Identify the blood parasite species.
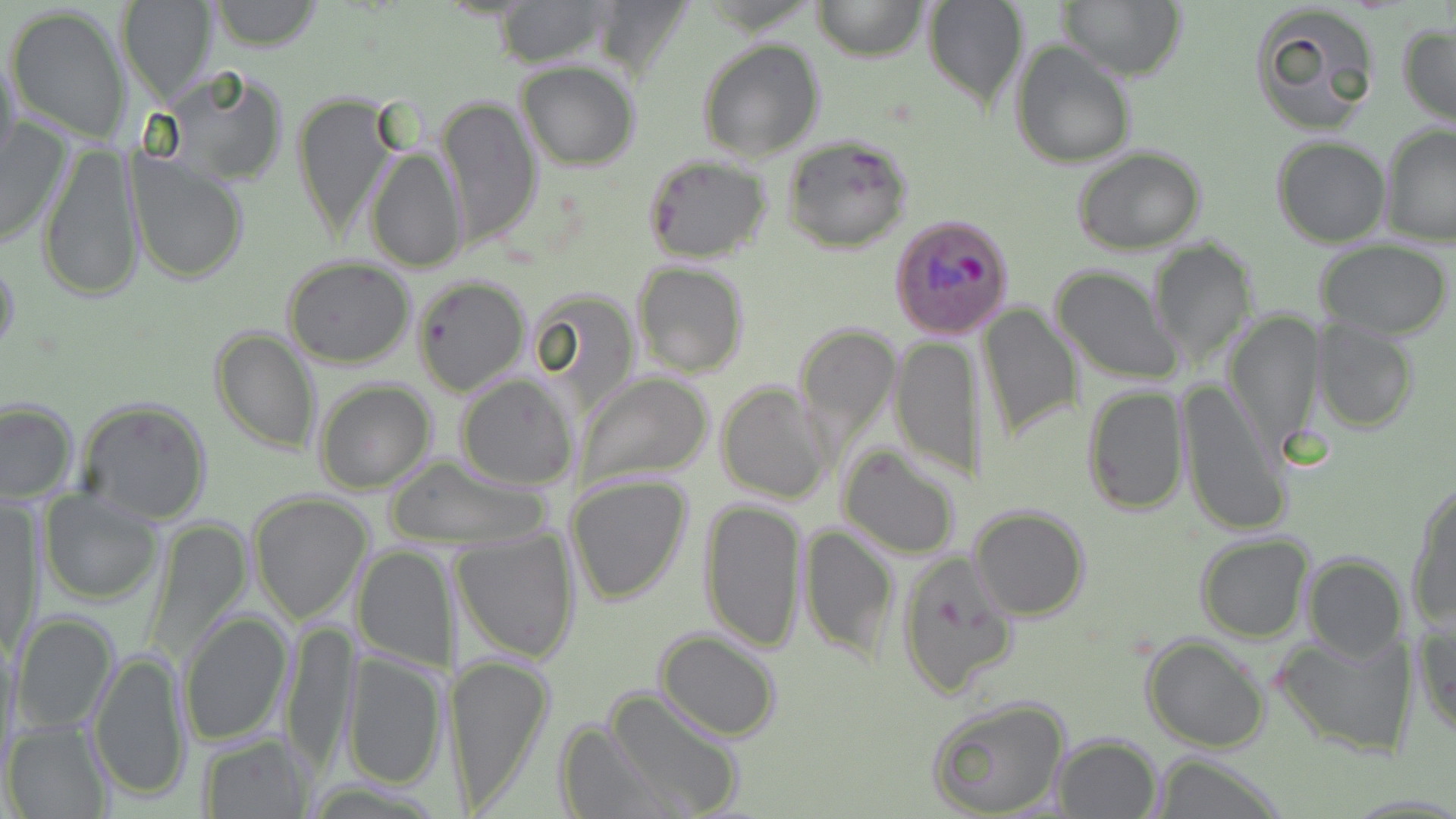

Plasmodium ovale.

modality = optical microscopy
image size = 1456×819 pixels
Plasmodium ovale-infected red blood cell locations = approximate bounding boxes as (x1, y1, x2, y2) in pixels: (891, 214, 1014, 339)
magnification = 1000x
field of view = single
preparation = thin blood film
stain = May-Grünwald-Giemsa
uninfected red blood cell locations = approximate bounding boxes as (x1, y1, x2, y2) in pixels: (207, 0, 328, 51), (493, 0, 613, 66), (588, 0, 696, 84), (812, 0, 927, 62), (920, 0, 1030, 111), (1055, 0, 1187, 83), (117, 1, 217, 105), (1248, 1, 1382, 135), (7, 5, 131, 143), (1398, 23, 1456, 127), (696, 38, 824, 163), (1011, 39, 1138, 168), (0, 44, 23, 184), (517, 62, 639, 169), (149, 65, 289, 189), (292, 93, 397, 241), (436, 95, 541, 246), (0, 117, 72, 250), (1380, 124, 1456, 246), (780, 133, 913, 254), (1270, 135, 1391, 247), (38, 139, 144, 303), (365, 147, 468, 274), (1072, 147, 1206, 256), (127, 151, 250, 283), (644, 154, 772, 264), (1150, 237, 1259, 367), (1314, 242, 1455, 339), (0, 246, 21, 371), (282, 258, 415, 369), (632, 261, 749, 378), (1052, 265, 1183, 384), (412, 273, 532, 396), (531, 290, 642, 411), (976, 302, 1081, 445), (1225, 310, 1323, 451), (1312, 318, 1419, 432), (794, 322, 902, 448), (209, 325, 320, 455), (891, 334, 983, 481), (574, 371, 714, 490), (455, 373, 580, 490), (1175, 375, 1289, 538), (313, 380, 436, 495), (715, 380, 834, 503), (1082, 385, 1189, 516), (76, 396, 214, 525), (0, 400, 79, 503), (838, 444, 962, 559), (385, 456, 552, 551), (566, 474, 693, 607), (1408, 484, 1456, 630), (40, 489, 163, 605), (247, 491, 374, 623), (698, 496, 807, 654), (1, 497, 40, 660), (968, 504, 1091, 622), (144, 516, 254, 668), (798, 522, 897, 661), (451, 527, 580, 665), (1194, 534, 1314, 643), (352, 542, 456, 672), (895, 548, 1020, 700), (1302, 552, 1405, 663), (177, 610, 294, 747), (10, 611, 120, 735), (1413, 617, 1455, 740), (281, 619, 358, 776), (1273, 629, 1418, 757), (655, 630, 782, 743), (1142, 634, 1270, 753), (87, 646, 197, 804), (445, 651, 555, 813), (341, 653, 447, 791), (600, 687, 744, 818), (928, 695, 1071, 817), (3, 718, 112, 819), (554, 721, 678, 817), (198, 733, 315, 816), (1052, 733, 1162, 817), (1149, 752, 1287, 818)